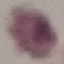

Summary:
  - Malaria status: uninfected
  - Stain: Giemsa
  - Capture: smartphone through the microscope eyepiece
  - Image type: automatically extracted cell patch, resized to 64 × 64 pixels
  - Preparation: thin smear